Describe the morphology of the red blood cells.
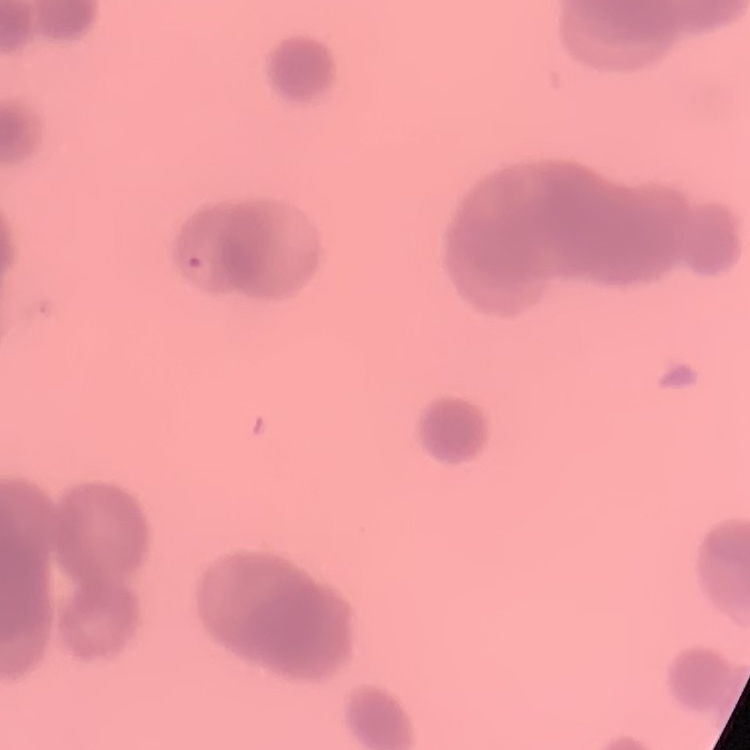
They show rouleaux formation.

preparation = thin blood film
stain = Field's or Giemsa
image type = square crop of a larger photomicrograph